Assess this cell for malaria.
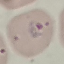

It is parasitized.

Acquired by smartphone through the microscope eyepiece. Thin blood film. Giemsa stain. Automatically extracted cell patch, resized to 64 × 64 pixels.